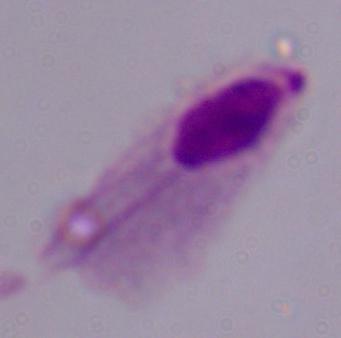
modality: photomicrograph
identification: trichomonad
magnification: 1000x